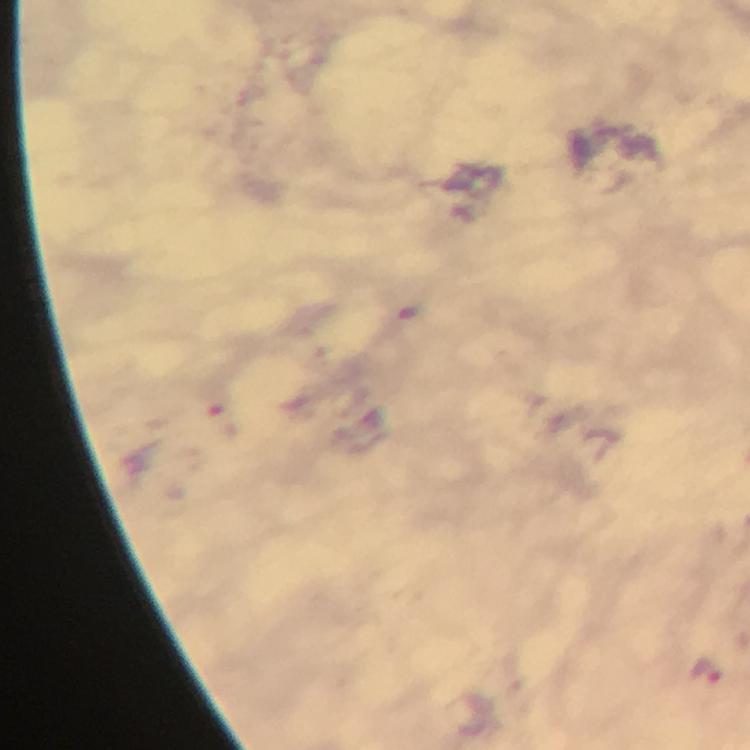
{
  "preparation": "thick blood smear",
  "stain": "Giemsa",
  "immersion_oil": "applied",
  "image_size": "750×750 pixels",
  "context": "from a diagnostic examination for malaria",
  "capture": "smartphone photograph through a microscope",
  "magnification": "100x",
  "cropped_from": "one field of view",
  "malaria_parasite_locations": "approximate centers as [x, y] in pixels: [706, 675]"
}